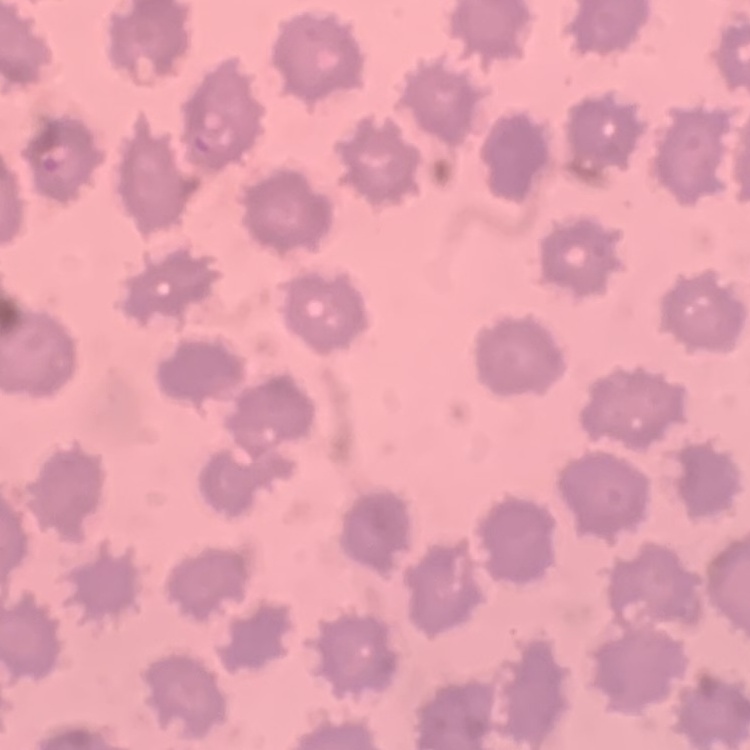
Summary:
  - Erythrocyte morphology: no rouleaux formation
  - Image type: one tile cut from a larger photomicrograph
  - Stain: Field's or Giemsa
  - Preparation: thin blood film